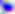
Toxoplasma gondii is seen. 400x magnification. Photomicrograph.